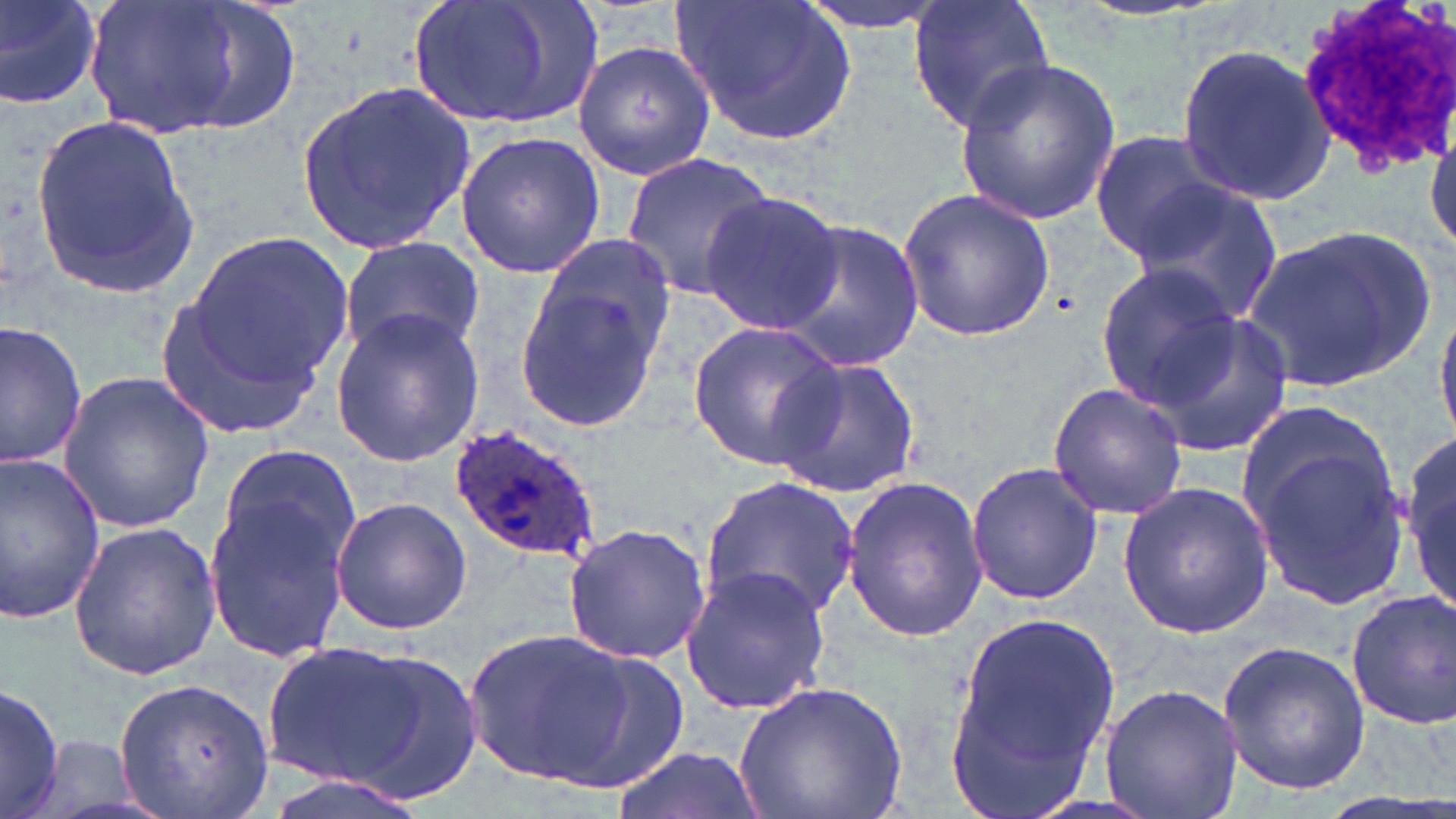
Plasmodium ovale-infected red blood cell locations = approximate bounding boxes as named x1/y1/x2/y2 corners in pixels: (x1=449, y1=424, x2=603, y2=563)
slide-level diagnosis = Plasmodium ovale
modality = light microscopy
white blood cell locations = approximate bounding boxes as named x1/y1/x2/y2 corners in pixels: (x1=1295, y1=0, x2=1456, y2=171)
field of view = single
magnification = 1000x
uninfected red blood cell locations = approximate bounding boxes as named x1/y1/x2/y2 corners in pixels: (x1=0, y1=0, x2=103, y2=111), (x1=75, y1=0, x2=293, y2=142), (x1=407, y1=0, x2=606, y2=130), (x1=672, y1=0, x2=858, y2=146), (x1=794, y1=0, x2=954, y2=36), (x1=906, y1=0, x2=1057, y2=133), (x1=572, y1=36, x2=721, y2=180), (x1=1174, y1=41, x2=1335, y2=208), (x1=953, y1=59, x2=1121, y2=225), (x1=296, y1=83, x2=476, y2=256), (x1=1425, y1=108, x2=1456, y2=267), (x1=31, y1=112, x2=200, y2=300), (x1=1088, y1=129, x2=1232, y2=259), (x1=455, y1=130, x2=605, y2=279), (x1=621, y1=152, x2=776, y2=301), (x1=1129, y1=181, x2=1285, y2=328), (x1=896, y1=185, x2=1058, y2=342), (x1=702, y1=192, x2=845, y2=337), (x1=778, y1=220, x2=924, y2=371), (x1=1244, y1=226, x2=1434, y2=393), (x1=187, y1=232, x2=352, y2=387), (x1=338, y1=236, x2=485, y2=361), (x1=512, y1=243, x2=679, y2=435), (x1=1096, y1=263, x2=1242, y2=406), (x1=153, y1=280, x2=336, y2=443), (x1=1431, y1=293, x2=1456, y2=449), (x1=1148, y1=306, x2=1294, y2=455), (x1=328, y1=309, x2=484, y2=466), (x1=1, y1=319, x2=91, y2=471), (x1=683, y1=320, x2=847, y2=472), (x1=767, y1=351, x2=923, y2=502), (x1=56, y1=372, x2=219, y2=534), (x1=1047, y1=383, x2=1188, y2=521), (x1=1237, y1=416, x2=1409, y2=607), (x1=1403, y1=434, x2=1456, y2=620), (x1=212, y1=442, x2=363, y2=583), (x1=0, y1=456, x2=107, y2=624), (x1=966, y1=460, x2=1102, y2=605), (x1=203, y1=475, x2=359, y2=665), (x1=698, y1=475, x2=861, y2=626), (x1=842, y1=476, x2=990, y2=643), (x1=1118, y1=480, x2=1276, y2=641), (x1=330, y1=497, x2=473, y2=635), (x1=67, y1=521, x2=223, y2=681), (x1=561, y1=522, x2=710, y2=665), (x1=680, y1=563, x2=831, y2=716), (x1=1350, y1=591, x2=1456, y2=730), (x1=945, y1=610, x2=1118, y2=811), (x1=466, y1=626, x2=638, y2=788), (x1=260, y1=637, x2=483, y2=803), (x1=1217, y1=641, x2=1371, y2=794), (x1=116, y1=678, x2=273, y2=817), (x1=1, y1=679, x2=66, y2=819), (x1=734, y1=681, x2=911, y2=819), (x1=1098, y1=683, x2=1244, y2=819), (x1=30, y1=734, x2=153, y2=819), (x1=608, y1=746, x2=765, y2=819), (x1=257, y1=770, x2=438, y2=819)
image size = 1456×819 pixels
stain = May-Grünwald-Giemsa
preparation = thin blood smear